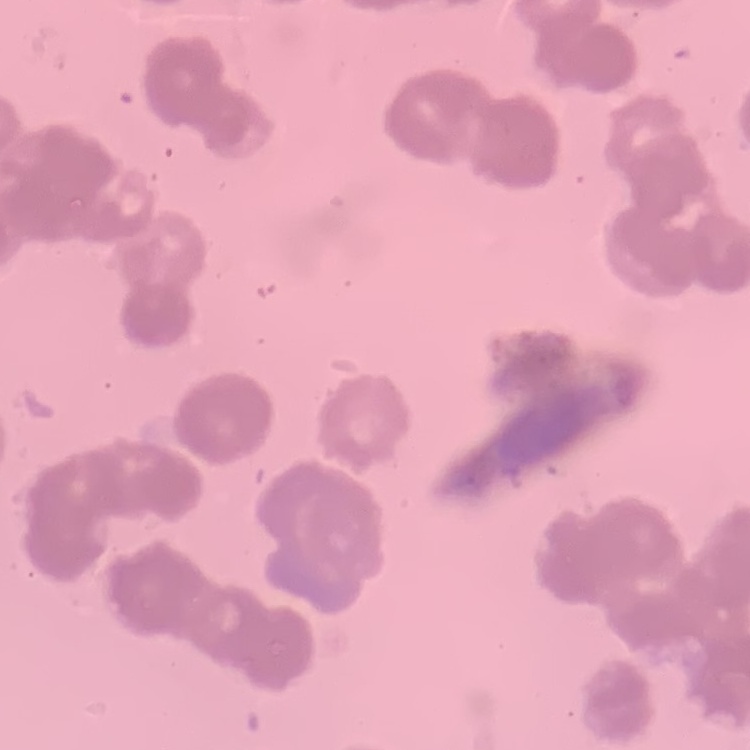

erythrocyte morphology = rouleaux formation
image type = one tile cut from a larger photomicrograph
stain = Field's or Giemsa
preparation = thin peripheral smear